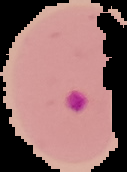
result = Plasmodium parasites identified
image size = 127×172 pixels
preparation = thin blood film
image type = cell region segmented out of the field of view; surrounding area masked to black